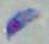
Toxoplasma gondii is shown. Micrograph. Captured at 1000x magnification.